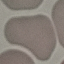
malaria status = uninfected
preparation = thin blood smear
stain = Giemsa
capture = smartphone camera at the microscope eyepiece
image type = cell patch, automatically extracted from a larger field of view and resized to 64 × 64 pixels